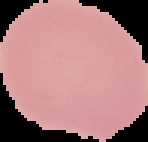
image_size: 148×142 pixels
preparation: thin blood smear
image_type: segmented cell region with the area outside set to black
result: no Plasmodium parasites seen